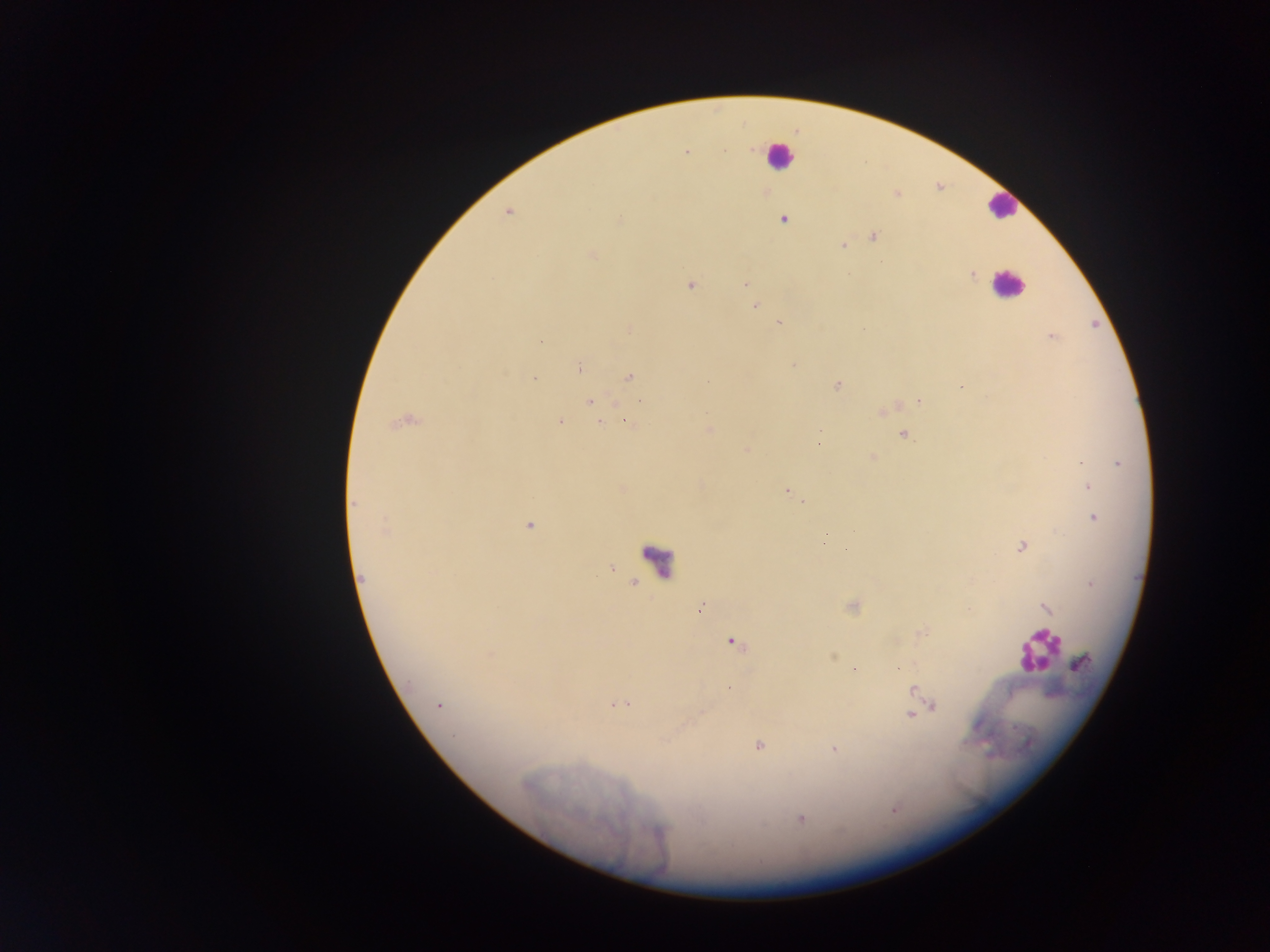 Approximate centers as [x, y] in pixels. Malaria parasite locations: [686, 151], [724, 151], [897, 194], [508, 212], [783, 219], [620, 220], [874, 236], [842, 246], [591, 255], [972, 275], [744, 284], [690, 285], [755, 305], [779, 324], [630, 330], [1052, 336], [541, 342], [793, 366], [580, 369], [629, 376], [533, 379], [836, 385], [962, 387], [640, 401], [919, 401], [590, 403], [881, 412], [627, 421], [403, 422], [560, 422], [600, 423], [709, 429], [820, 431], [904, 435], [746, 450], [872, 457], [1082, 462], [1118, 464], [1088, 487], [787, 491], [356, 502], [804, 502], [1093, 518], [528, 525], [384, 529], [824, 542], [1021, 547], [362, 578], [1090, 584], [1046, 607], [699, 610], [733, 642], [1081, 663], [854, 669], [729, 689], [913, 691], [618, 704], [439, 705], [933, 706], [910, 716], [759, 746], [834, 749], [800, 818]. Leukocyte locations: [779, 156], [1002, 206], [1007, 283], [658, 562], [1037, 650]. One field of view. Collected in Ghana. Photographed through a microscope with a mobile-phone camera. Image is 1270×952 pixels. Thick blood film.